Assess the morphology of the red blood cells.
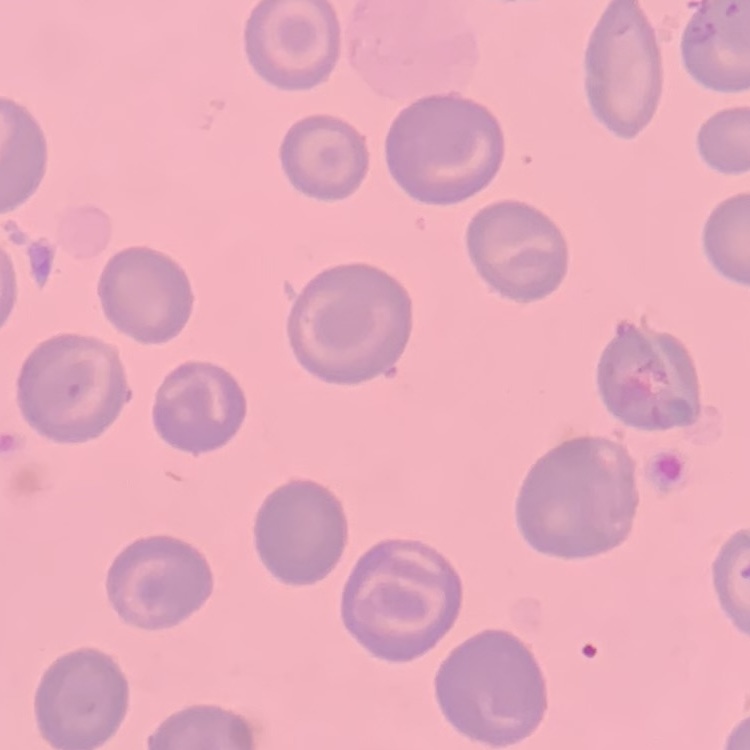
No rouleaux formation.

stain = Field's or Giemsa
image type = one tile cut from a larger photomicrograph
preparation = thin peripheral smear